State the blood parasite species.
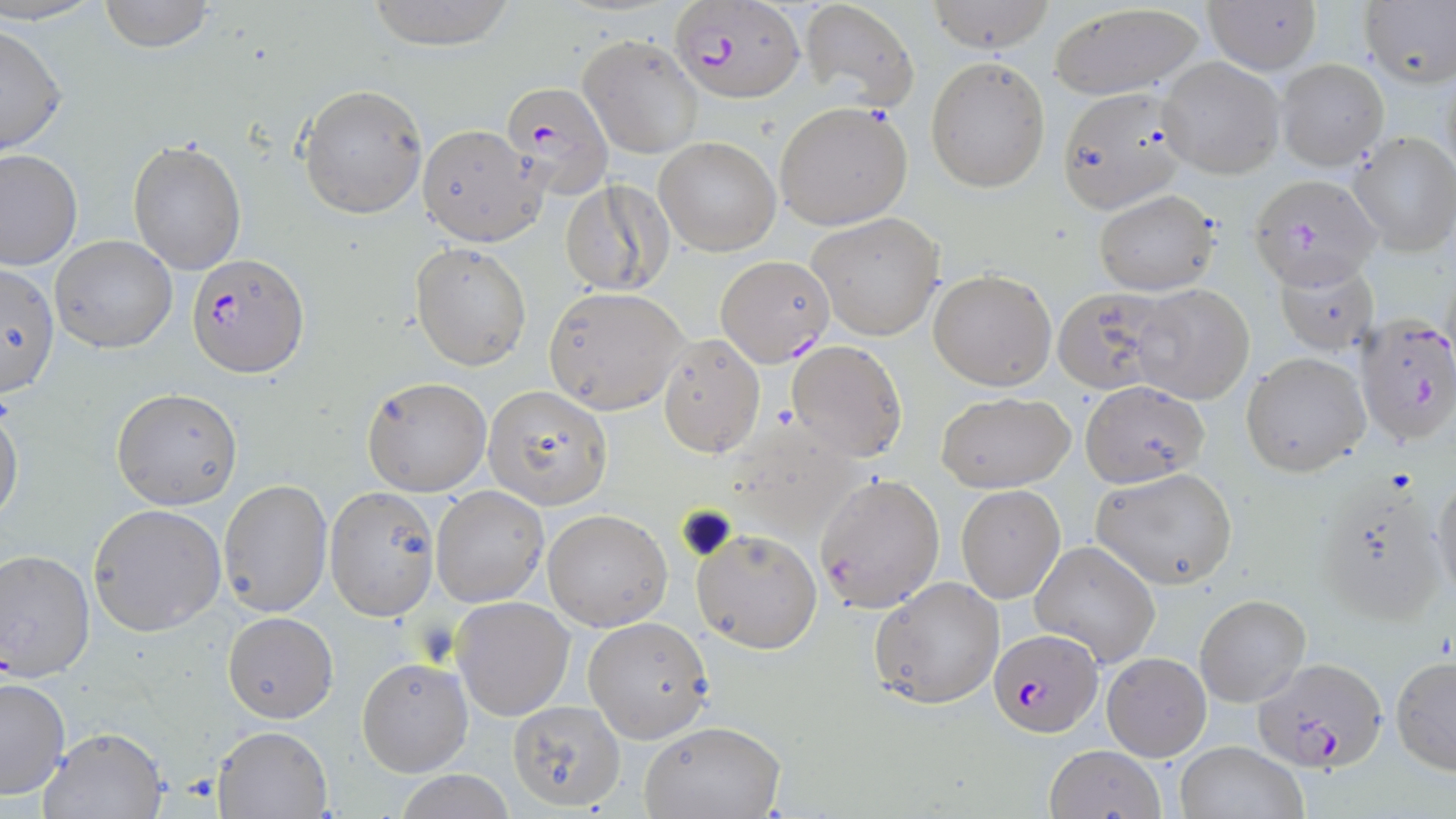
Plasmodium falciparum.

Summary:
  - Coordinate format: approximate bounding boxes as (x1, y1, x2, y2) in pixels
  - Plasmodium falciparum-infected red blood cell locations: (673, 4, 804, 103), (501, 81, 614, 201), (1250, 174, 1382, 290), (188, 253, 306, 376), (716, 255, 833, 367), (1356, 314, 1456, 447), (989, 629, 1102, 739), (1251, 656, 1387, 777)
  - Uninfected red blood cell locations: (97, 0, 218, 52), (365, 0, 520, 50), (925, 0, 1056, 53), (1205, 0, 1323, 76), (796, 1, 921, 110), (1357, 1, 1456, 88), (1045, 3, 1208, 101), (0, 20, 67, 157), (579, 33, 702, 159), (925, 55, 1050, 193), (1157, 56, 1286, 179), (1275, 59, 1389, 170), (298, 83, 428, 218), (1057, 86, 1191, 213), (775, 101, 912, 230), (415, 123, 545, 245), (1348, 130, 1455, 256), (655, 137, 780, 255), (127, 138, 247, 275), (0, 148, 82, 271), (560, 179, 674, 297), (1093, 189, 1220, 295), (807, 212, 946, 341), (51, 234, 178, 353), (411, 242, 530, 371), (1273, 256, 1380, 354), (0, 260, 61, 399), (927, 270, 1056, 391), (1132, 283, 1256, 405), (543, 286, 688, 414), (1052, 286, 1175, 396), (659, 334, 765, 458), (786, 340, 908, 462), (1241, 352, 1370, 478), (360, 376, 493, 497), (1081, 380, 1208, 487), (483, 385, 613, 509), (112, 388, 243, 512), (936, 391, 1076, 493), (0, 399, 22, 524), (1091, 467, 1238, 590), (1430, 470, 1456, 604), (813, 472, 945, 613), (219, 479, 333, 618), (1319, 482, 1448, 623), (956, 484, 1066, 603), (323, 485, 440, 619), (429, 486, 548, 607), (88, 503, 227, 636), (542, 507, 673, 631), (691, 527, 823, 653), (1029, 540, 1162, 668), (0, 547, 97, 681), (869, 575, 1005, 709), (1196, 594, 1311, 708), (452, 596, 575, 721), (222, 611, 337, 722), (583, 618, 710, 742), (1102, 652, 1211, 760), (1390, 654, 1456, 775), (356, 656, 473, 777), (0, 676, 71, 801), (511, 700, 623, 813), (640, 720, 787, 819), (214, 726, 332, 818), (37, 727, 167, 818), (1173, 740, 1308, 819), (1045, 743, 1165, 818)
  - Stain: May-Grünwald-Giemsa
  - Magnification: 1000x
  - Image size: 1456×819 pixels
  - Modality: light microscopy
  - Field of view: one of a larger specimen
  - Preparation: thin blood smear